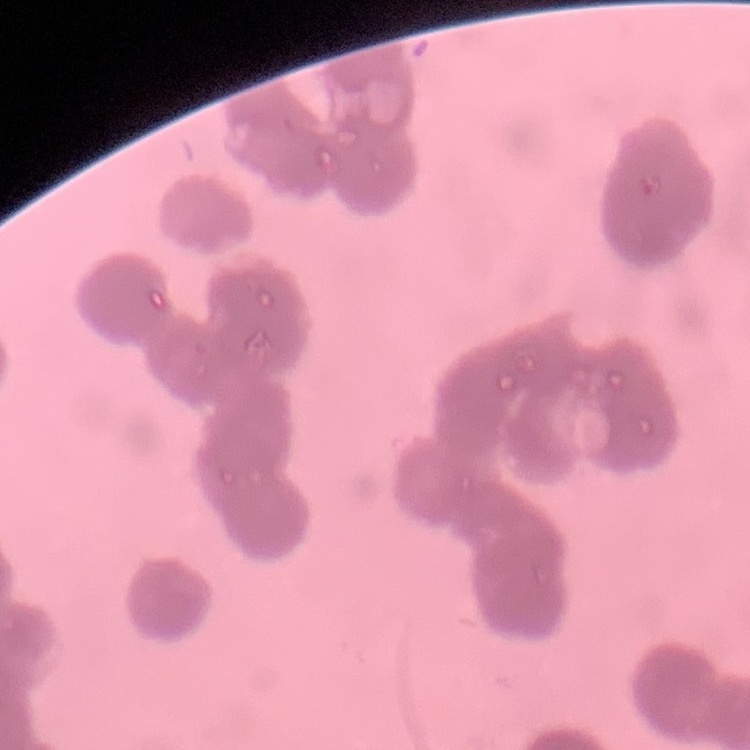
The erythrocytes exhibit rouleaux formation. One tile cut from a larger photomicrograph. Thin peripheral smear. Field's or Giemsa stain.